Name the blood parasite species.
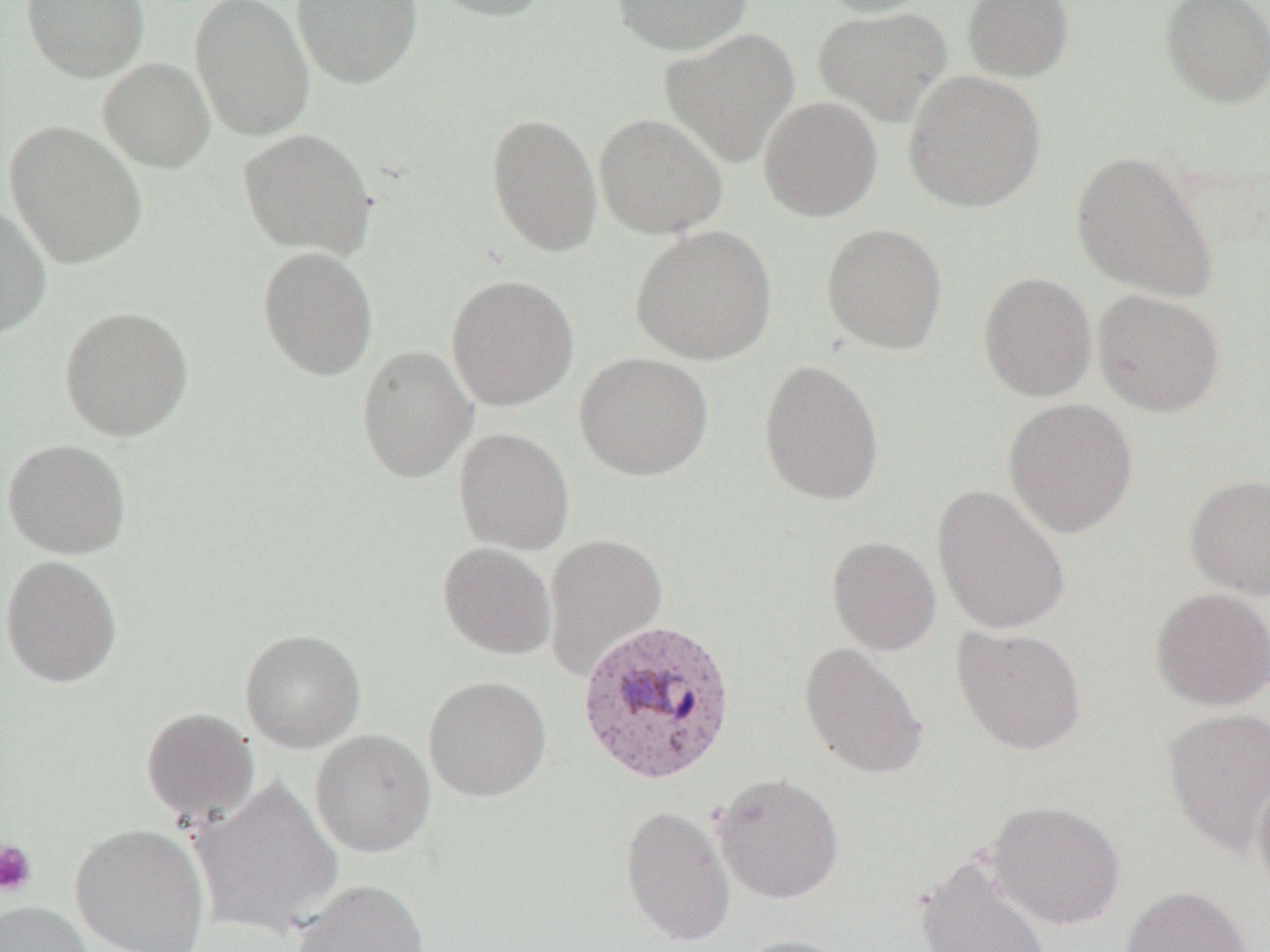
Plasmodium vivax.

Approximate bounding boxes as (x1, y1, x2, y2) in pixels. Uninfected red blood cell locations: (22, 0, 149, 82), (190, 0, 315, 141), (291, 0, 423, 87), (423, 0, 553, 21), (612, 0, 753, 55), (810, 0, 938, 18), (962, 0, 1075, 83), (1159, 0, 1270, 109), (813, 6, 952, 127), (661, 28, 800, 169), (98, 57, 215, 172), (903, 70, 1047, 212), (758, 96, 883, 222), (486, 113, 603, 257), (594, 113, 729, 239), (4, 120, 148, 268), (238, 127, 376, 258), (1071, 151, 1219, 303), (0, 203, 52, 338), (821, 223, 948, 355), (630, 225, 778, 365), (257, 246, 378, 380), (978, 271, 1098, 402), (446, 274, 579, 410), (1092, 290, 1225, 417), (59, 306, 193, 441), (357, 345, 477, 484), (574, 352, 714, 481), (758, 359, 885, 506), (1003, 398, 1138, 538), (454, 427, 575, 555), (2, 438, 132, 559), (1185, 474, 1270, 600), (933, 485, 1070, 635), (543, 533, 668, 679), (827, 536, 941, 656), (437, 542, 557, 660), (0, 554, 123, 688), (1151, 588, 1270, 711), (952, 626, 1086, 755), (240, 629, 366, 753), (799, 642, 928, 780), (423, 675, 552, 802), (140, 707, 260, 826), (1161, 707, 1270, 858), (310, 729, 435, 858), (712, 772, 845, 905), (1251, 772, 1270, 901), (189, 777, 345, 939), (987, 800, 1126, 931), (620, 804, 737, 948), (69, 823, 212, 952), (915, 855, 1053, 951), (290, 878, 430, 952), (1121, 885, 1253, 952), (0, 901, 96, 952), (730, 935, 855, 952). Plasmodium vivax-infected red blood cell locations: (576, 619, 738, 786). Platelet locations: (0, 840, 38, 897). Optical microscopy. One field of a larger specimen. Captured at 1000x magnification. Image is 1270×952 pixels. Thin blood film.